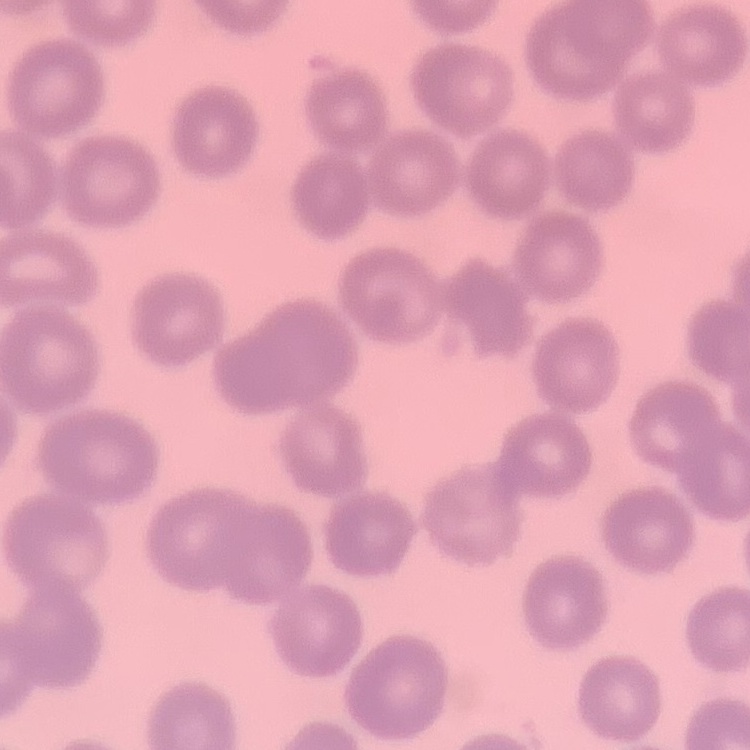 The erythrocytes exhibit no rouleaux formation. Field's or Giemsa stain. Thin peripheral smear. One tile cut from a larger photomicrograph.